Identify the preparation type.
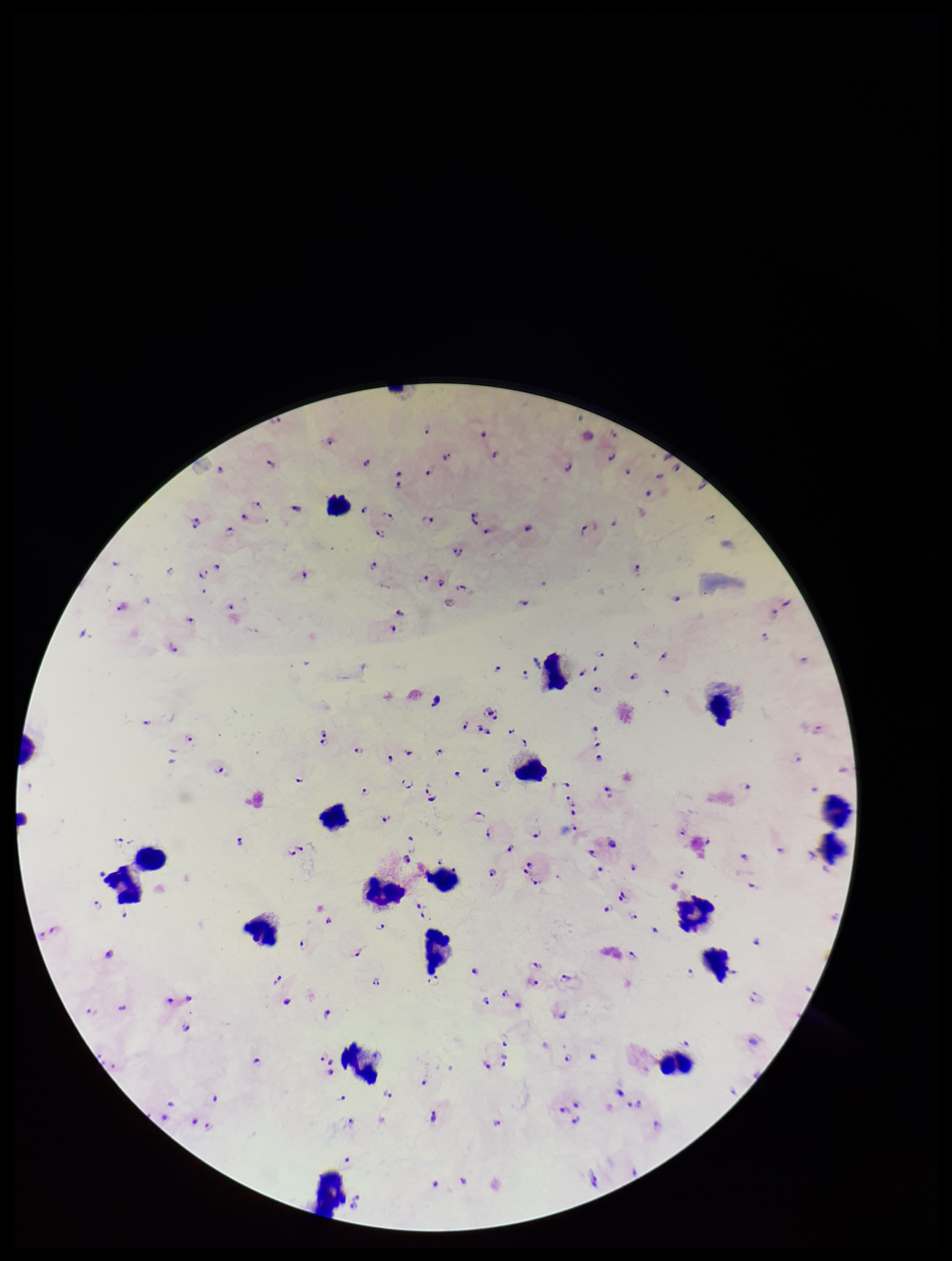

Thick.

Summary:
  - Parasite count: 117
  - Leukocyte count: 19
  - Capture: smartphone photograph through the microscope eyepiece
  - Image size: 952×1261 pixels
  - Plasmodium parasites: detected
  - Patient malaria status: positive
  - Field of view: one from this slide
  - Species reported for this patient: Plasmodium falciparum
  - Stain: Giemsa